Classify this cell by malaria status.
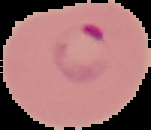

Parasitized.

From a thin blood film. Image is 151×130 pixels. Segmented cell region on a black background.